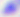

Micrograph. Toxoplasma gondii is shown. 400x magnification.